Report the malaria status of this cell.
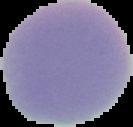

It is uninfected.

Summary:
  - Preparation: thin blood smear
  - Image size: 133×127 pixels
  - Image type: cell region segmented out of the field of view; surrounding area masked to black